Comment on the morphology of the erythrocytes.
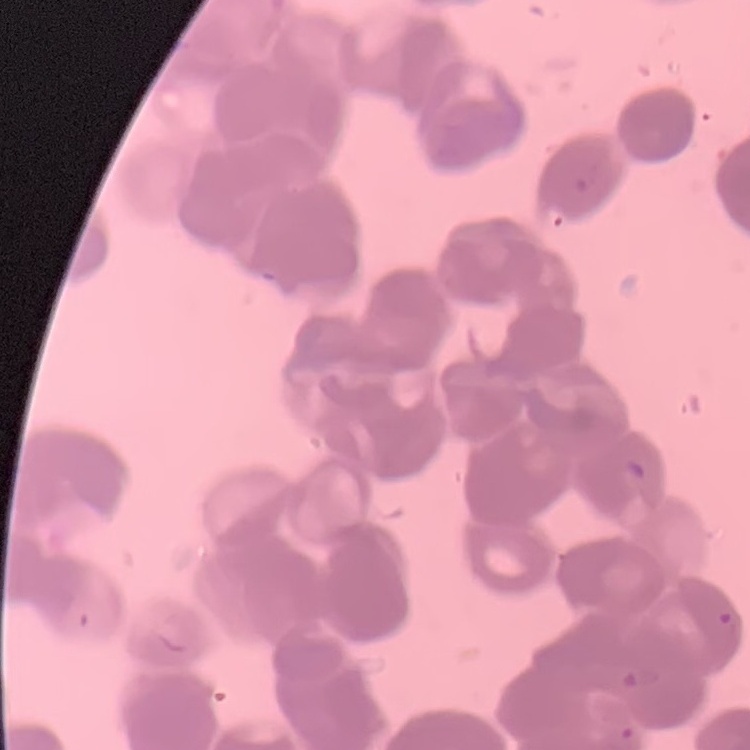

Rouleaux formation.

Summary:
  - Stain: Field's or Giemsa
  - Preparation: thin blood smear
  - Image type: square crop of a larger photomicrograph